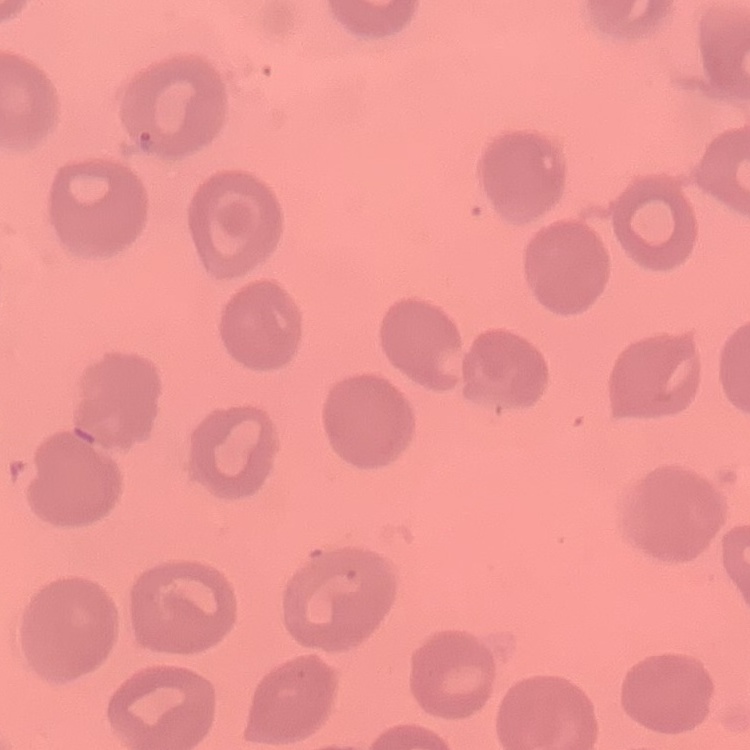

The erythrocytes show no rouleaux formation. Square crop of a larger photomicrograph. Field's or Giemsa stain. Thin blood film.